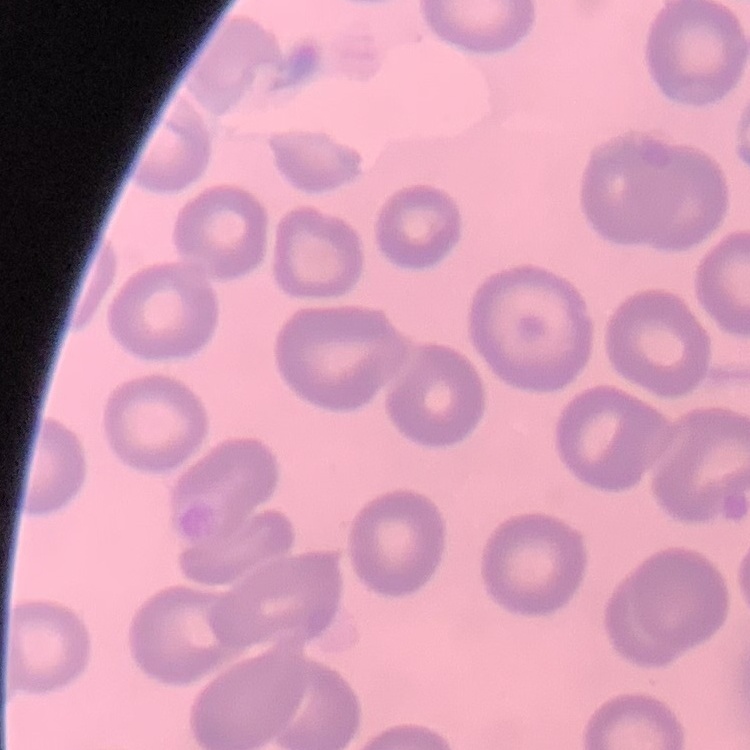
The red blood cells show no rouleaux formation. One tile cut from a larger photomicrograph. Thin peripheral smear. Stained with either Field's or Giemsa.